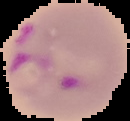
From a thin blood smear. Image is 130×121 pixels. Malaria status: parasitized. Cell region segmented out of the field of view; the surrounding area is masked to black.